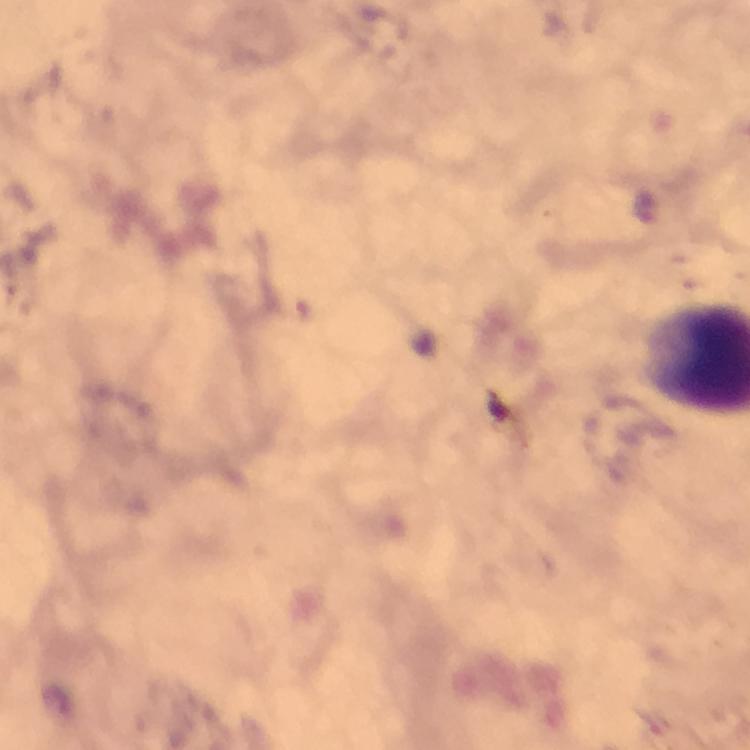

Approximate centers as (x, y) in pixels. Plasmodium parasite locations: (646, 208). Thick blood smear. 100x magnification. Photographed through the microscope with a smartphone camera. Image is 750×750 pixels. Immersion oil was used. From a malaria diagnostic workup. Giemsa stain. Cropped region of a single field of view.